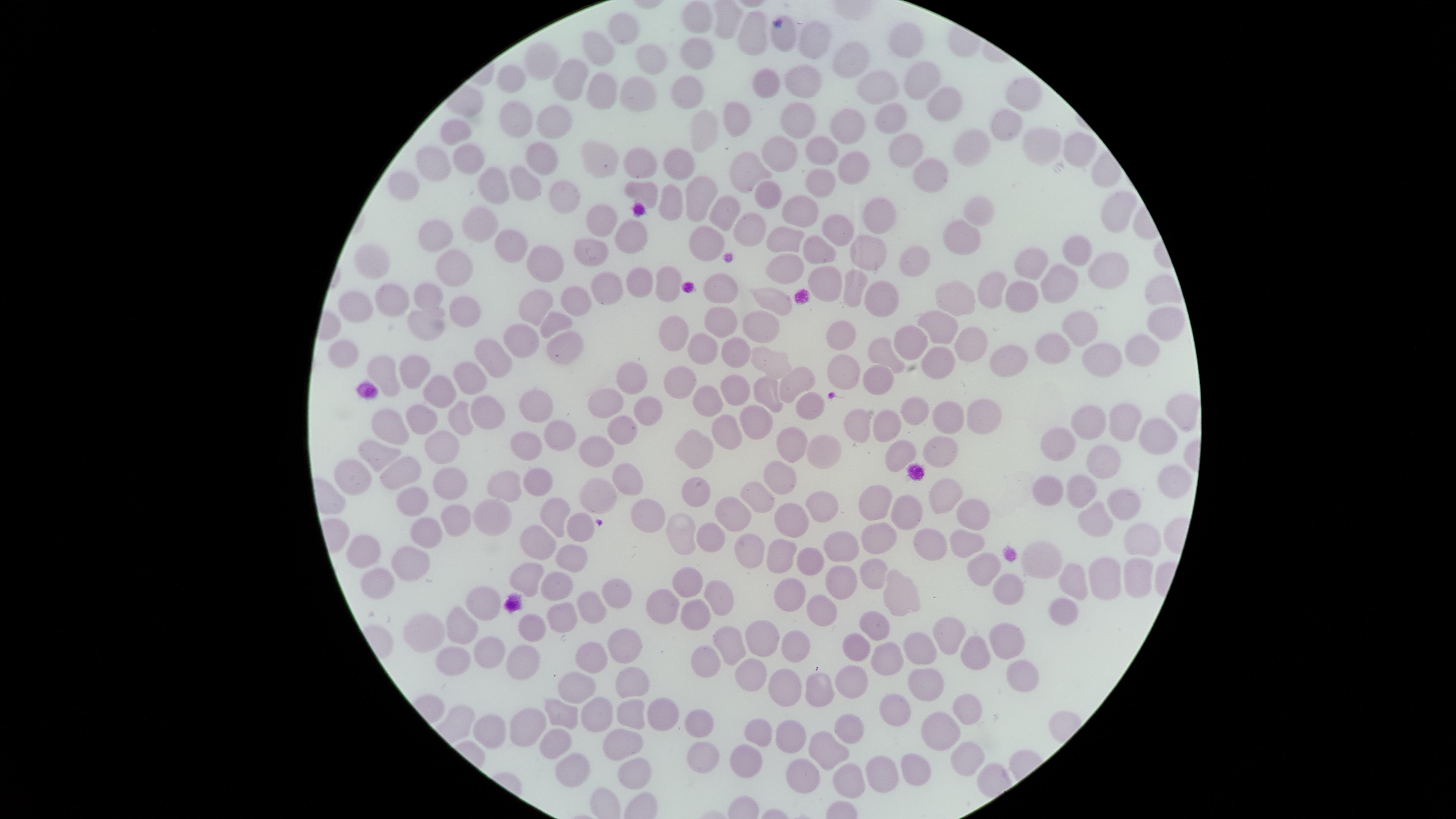

capture: smartphone photograph through the microscope eyepiece
preparation: thin blood film
visible_region: circular
field_of_view: single
stain: Giemsa
uninfected_RBCs: 'approximate marker points as {x, y} in pixels: {690, 12}, {620, 28}, {753, 33}, {782, 35}, {903, 36}, {808, 40}, {600, 45}, {695, 53}, {851, 54}, {647, 55}, {539, 63}, {921, 72}, {570, 75}, {512, 77}, {796, 78}, {874, 78}, {761, 80}, {687, 86}, {599, 91}, {1020, 91}, {636, 93}, {945, 102}, {736, 114}, {513, 116}, {892, 116}, {556, 119}, {794, 121}, {998, 122}, {704, 125}, {846, 129}, {456, 133}, {1043, 146}, {971, 149}, {776, 150}, {1077, 150}, {820, 152}, {900, 152}, {542, 153}, {465, 158}, {602, 159}, {642, 160}, {427, 162}, {682, 165}, {853, 166}, {749, 169}, {935, 178}, {817, 179}, {524, 181}, {494, 183}, {399, 189}, {767, 189}, {641, 190}, {569, 191}, {697, 197}, {666, 202}, {980, 206}, {733, 207}, {796, 207}, {872, 210}, {1113, 212}, {598, 217}, {479, 223}, {839, 225}, {748, 228}, {961, 235}, {437, 237}, {624, 237}, {780, 237}, {700, 242}, {510, 247}, {817, 247}, {1075, 248}, {589, 249}, {864, 249}, {917, 251}, {1027, 258}, {548, 260}, {371, 261}, {787, 266}, {454, 268}, {1104, 268}, {1053, 275}, {823, 276}, {639, 279}, {666, 280}, {986, 283}, {604, 285}, {724, 286}, {854, 286}, {421, 289}, {1024, 291}, {773, 297}, {386, 298}, {356, 299}, {573, 299}, {533, 300}, {954, 300}, {887, 301}, {463, 303}, {428, 317}, {556, 320}, {722, 321}, {1167, 323}, {756, 324}, {673, 326}, {937, 326}, {1081, 328}, {835, 333}, {908, 334}, {971, 340}, {525, 341}, {565, 343}, {884, 346}, {1045, 346}, {701, 347}, {1143, 347}, {737, 349}, {351, 350}, {1106, 356}, {502, 358}, {1005, 358}, {770, 361}, {931, 361}, {384, 369}, {847, 369}, {417, 374}, {474, 375}, {880, 378}, {678, 379}, {635, 380}, {796, 382}, {732, 383}, {441, 391}, {768, 392}, {704, 393}, {806, 397}, {607, 401}, {533, 402}, {650, 403}, {426, 409}, {911, 409}, {487, 410}, {1180, 411}, {760, 415}, {945, 416}, {980, 416}, {459, 417}, {858, 418}, {1094, 418}, {386, 419}, {1126, 419}, {886, 423}, {621, 426}, {725, 429}, {559, 434}, {1060, 434}, {1154, 435}, {791, 442}, {443, 445}, {528, 446}, {597, 447}, {696, 447}, {378, 449}, {823, 449}, {896, 451}, {937, 454}, {1094, 459}, {407, 470}, {778, 472}, {626, 475}, {351, 477}, {533, 480}, {447, 482}, {1164, 483}, {499, 485}, {1050, 485}, {698, 487}, {1082, 487}, {597, 489}, {757, 493}, {941, 495}, {412, 499}, {875, 501}, {1121, 502}, {820, 504}, {910, 505}, {649, 506}, {554, 512}, {731, 512}, {451, 513}, {483, 515}, {1097, 515}, {969, 516}, {788, 519}, {578, 526}, {423, 530}, {675, 534}, {884, 536}, {704, 538}, {923, 538}, {1132, 543}, {846, 544}, {540, 545}, {365, 547}, {750, 547}, {961, 550}, {784, 556}, {569, 558}, {985, 559}, {1041, 560}, {404, 563}, {810, 566}, {872, 566}, {1100, 572}, {529, 574}, {1130, 576}, {841, 577}, {375, 578}, {1068, 579}, {554, 584}, {1011, 584}, {679, 585}, {897, 587}, {611, 594}, {788, 596}, {720, 597}, {480, 603}, {661, 606}, {823, 606}, {1062, 606}, {588, 609}, {697, 609}, {560, 616}, {458, 622}, {872, 627}, {415, 629}, {530, 629}, {762, 634}, {733, 635}, {949, 635}, {1000, 635}, {789, 643}, {918, 644}, {629, 645}, {488, 647}, {852, 647}, {886, 652}, {972, 652}, {707, 659}, {444, 660}, {523, 660}, {586, 662}, {750, 673}, {854, 678}, {1024, 678}, {924, 684}, {630, 685}, {781, 687}, {572, 690}, {809, 692}, {891, 706}, {965, 706}, {601, 710}, {563, 712}, {634, 712}, {658, 712}, {699, 721}, {522, 725}, {850, 725}, {493, 729}, {788, 729}, {935, 729}, {758, 733}, {623, 735}, {548, 742}, {828, 742}, {701, 750}, {749, 756}, {961, 757}, {876, 765}, {912, 765}, {572, 770}, {802, 771}, {846, 771}, {633, 775}'
image_size: 1456×819 pixels
presence: no malaria parasites detected